Identify the cell.
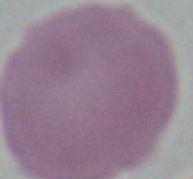

An erythrocyte.

Captured at 1000x magnification. Micrograph.